Point out each leukocyte.
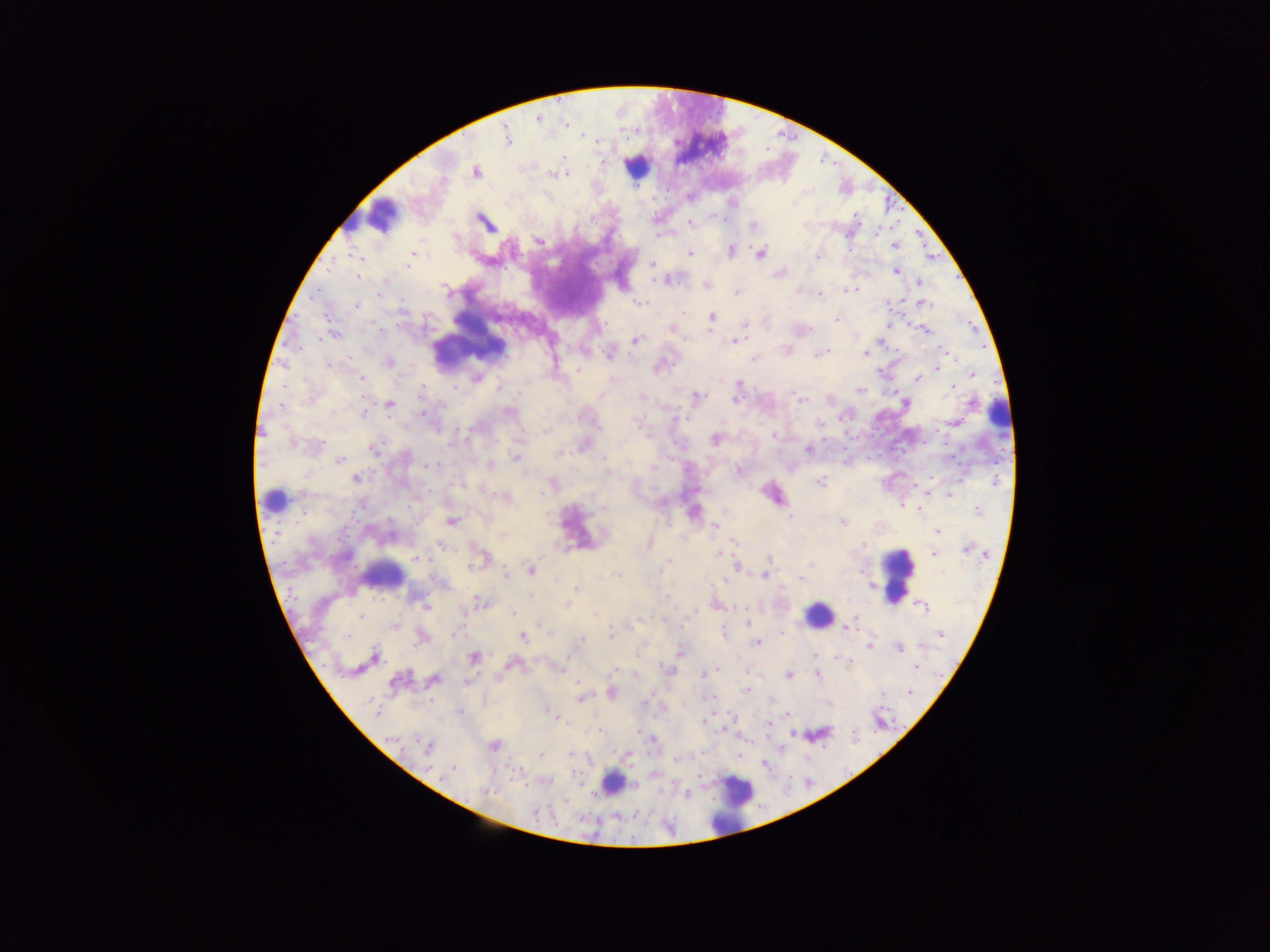
Approximate centers as [x, y] in pixels.
Leukocytes: [636, 167], [389, 215], [352, 220], [471, 336], [997, 415], [273, 500], [384, 574], [897, 574], [819, 615], [614, 782], [733, 803].

Malaria parasite locations: [538, 119], [507, 136], [583, 136], [564, 157], [604, 162], [476, 172], [553, 174], [714, 218], [484, 222], [690, 223], [753, 225], [878, 230], [657, 236], [539, 241], [895, 245], [731, 251], [690, 253], [761, 253], [412, 255], [818, 255], [358, 256], [361, 258], [652, 264], [408, 266], [330, 269], [895, 271], [779, 273], [358, 276], [655, 279], [661, 280], [667, 280], [919, 282], [707, 286], [447, 289], [799, 290], [849, 290], [737, 292], [379, 294], [820, 294], [901, 300], [638, 302], [885, 303], [926, 304], [357, 306], [684, 313], [712, 317], [836, 319], [745, 324], [888, 325], [377, 329], [672, 330], [925, 330], [334, 335], [635, 341], [733, 341], [942, 350], [898, 351], [826, 352], [820, 353], [866, 353], [609, 354], [754, 359], [389, 362], [328, 366], [938, 367], [657, 368], [578, 370], [879, 371], [973, 374], [361, 378], [476, 378], [917, 378], [455, 386], [952, 387], [498, 388], [422, 389], [860, 390], [697, 396], [642, 397], [736, 399], [801, 400], [972, 403], [390, 404], [282, 406], [442, 407], [423, 412], [509, 412], [363, 413], [954, 422], [637, 424], [820, 425], [599, 427], [471, 430], [547, 431], [775, 435], [715, 439], [294, 444], [374, 449], [808, 450], [559, 452], [516, 458], [605, 459], [340, 461], [489, 465], [433, 466], [654, 467], [739, 471], [606, 472], [930, 477], [355, 478], [820, 482], [995, 482], [950, 494], [902, 506], [604, 509], [919, 509], [977, 511], [789, 517], [451, 521], [843, 523], [715, 526], [937, 532], [735, 542], [648, 545], [442, 546], [863, 546], [967, 549], [717, 554], [932, 554], [417, 558], [769, 559], [811, 565], [666, 566], [737, 566], [805, 567], [532, 570], [662, 570], [861, 571], [941, 573], [506, 575], [617, 575], [765, 575], [801, 578], [724, 582], [575, 589], [529, 595], [668, 597], [482, 602], [567, 604], [717, 605], [425, 607], [922, 607], [514, 612], [361, 616], [855, 616], [641, 619], [748, 622], [634, 624], [395, 627], [846, 629], [782, 633], [454, 634], [611, 634], [941, 634], [724, 635], [347, 636], [422, 637], [523, 637], [582, 641], [757, 643], [870, 646], [900, 649], [639, 652], [680, 652], [814, 654], [375, 656], [473, 658], [839, 658], [850, 661], [510, 664], [916, 667], [668, 668], [558, 669], [717, 669], [614, 671], [707, 673], [703, 675], [788, 675], [817, 676], [434, 679], [397, 681], [467, 682], [579, 685], [746, 690], [910, 692], [611, 693], [712, 697], [581, 699], [644, 703], [376, 709], [460, 712], [551, 713], [789, 715], [731, 716], [557, 718], [703, 720], [768, 724], [599, 731], [639, 733], [793, 734], [393, 739], [653, 741], [494, 746], [428, 748], [571, 754], [541, 755], [676, 760], [454, 768], [487, 792], [686, 794], [536, 813]. Thick blood film. One field of view. Image is 1270×952 pixels. Photographed through a microscope with a mobile-phone camera. Sample from Ghana.